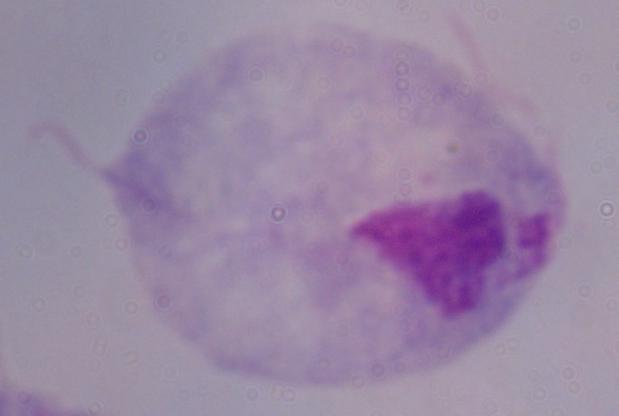
Summary:
  - Magnification: 1000x
  - Identification: trichomonad
  - Modality: micrograph